Assess this cell for malaria.
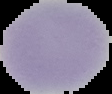
Uninfected.

image size = 112×94 pixels
preparation = thin blood smear
image type = segmented cell region on a black background